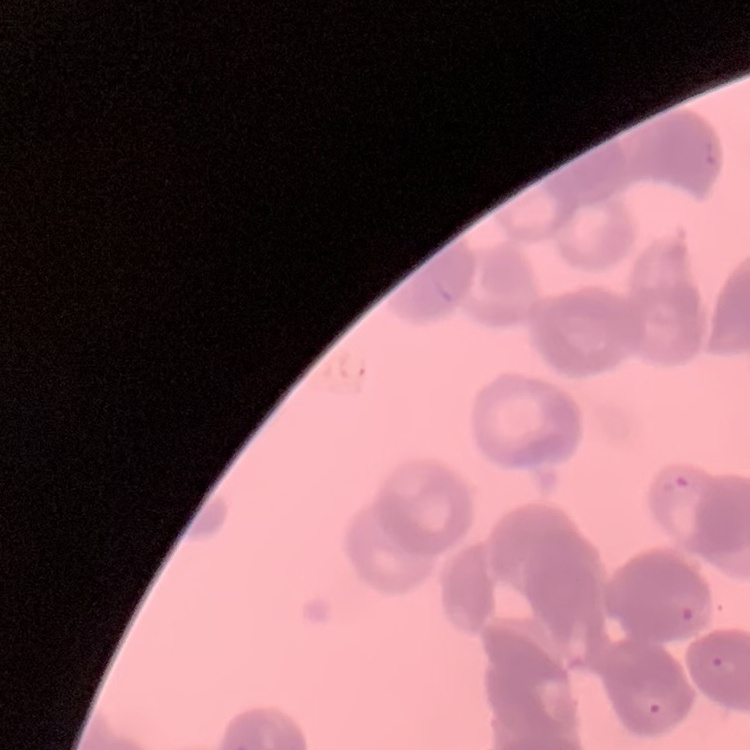

The erythrocytes exhibit rouleaux formation. Stained with either Field's or Giemsa. Thin blood film. Square crop of a larger photomicrograph.